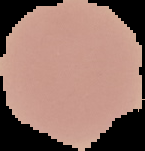
Segmented cell region on a black background. Image is 145×151 pixels. Malaria status: uninfected. From a thin blood smear.